Describe the morphology of the erythrocytes.
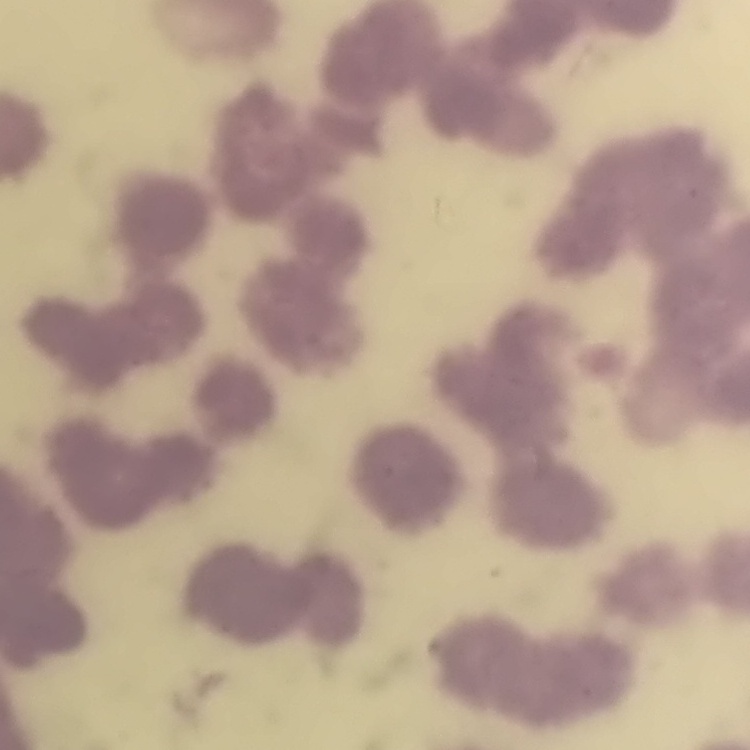

Rouleaux formation.

Field's or Giemsa stain. Thin blood smear. One tile cut from a larger photomicrograph.